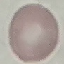

Summary:
  - Malaria status: uninfected
  - Image type: cell patch, automatically extracted from a larger field of view and resized to 64 × 64 pixels
  - Capture: smartphone through the microscope eyepiece
  - Preparation: thin smear
  - Stain: Giemsa